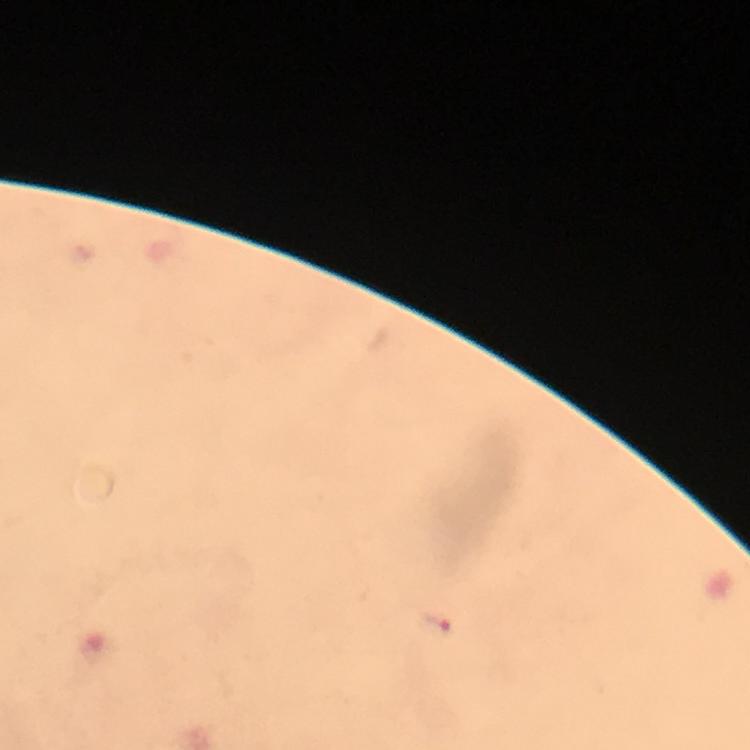

Approximate object centers, in pixels from the top-left corner.
Summary:
  - Malaria parasite locations: (x=437, y=624)
  - Stain: Giemsa
  - Image size: 750×750 pixels
  - Magnification: 100x
  - Context: from a malaria diagnostic workup
  - Cropped from: one field of view
  - Capture: smartphone camera through the microscope
  - Immersion oil: used
  - Preparation: thick blood film